Assess this cell for malaria.
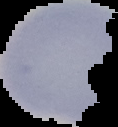
It is uninfected.

Summary:
  - Preparation: thin blood smear
  - Image size: 118×127 pixels
  - Image type: segmented cell region on a black background